Identify the blood parasite species.
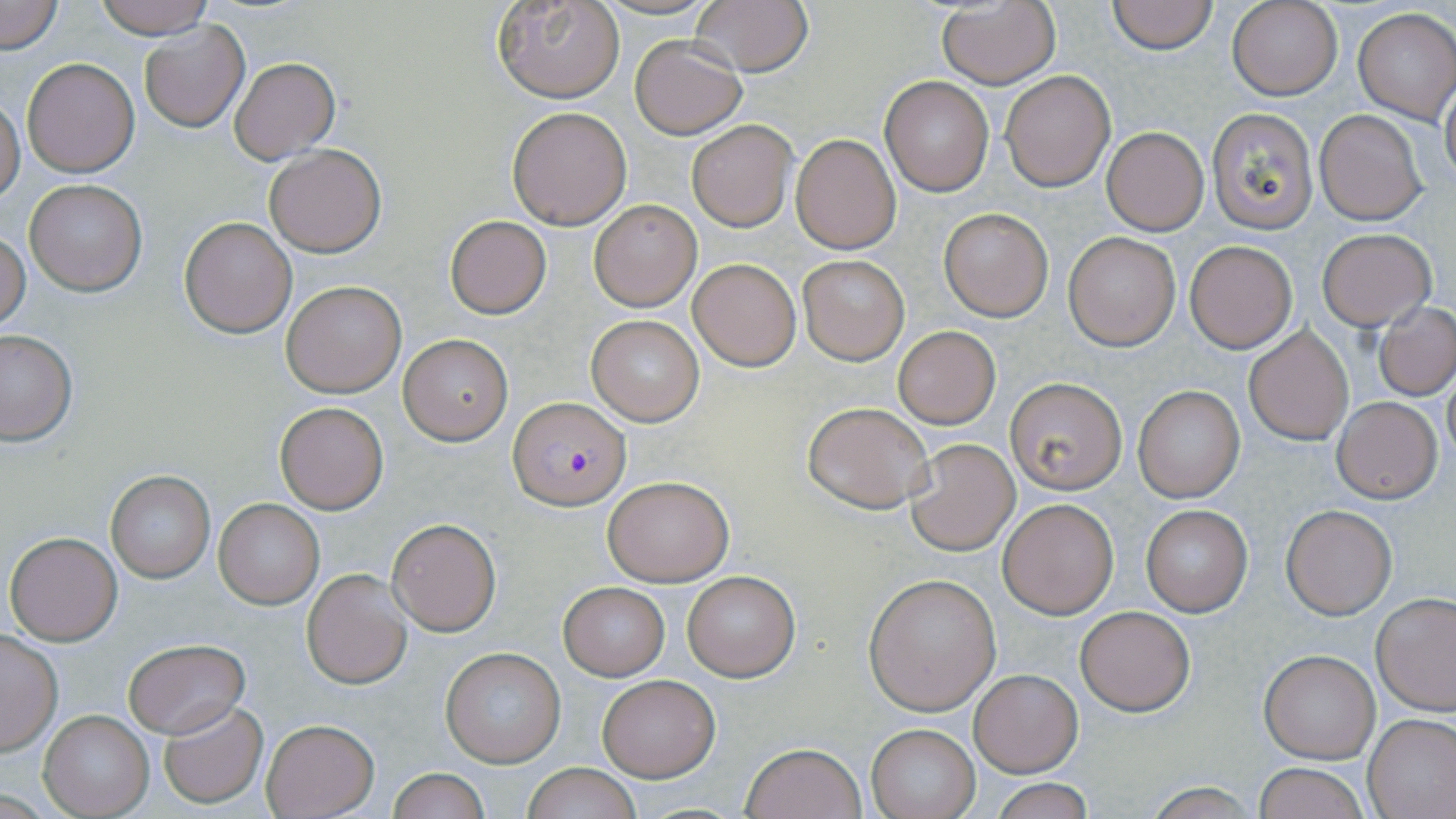
Plasmodium falciparum.

magnification = 1000x
uninfected red blood cell locations = approximate bounding boxes as named x1/y1/x2/y2 corners in pixels: (x1=1, y1=0, x2=65, y2=55), (x1=94, y1=0, x2=216, y2=40), (x1=1108, y1=0, x2=1216, y2=54), (x1=496, y1=1, x2=623, y2=103), (x1=690, y1=1, x2=814, y2=77), (x1=1227, y1=1, x2=1342, y2=100), (x1=937, y1=3, x2=1061, y2=87), (x1=1353, y1=8, x2=1455, y2=122), (x1=140, y1=21, x2=249, y2=132), (x1=630, y1=37, x2=747, y2=138), (x1=22, y1=58, x2=140, y2=176), (x1=230, y1=58, x2=339, y2=162), (x1=1001, y1=69, x2=1116, y2=192), (x1=880, y1=76, x2=995, y2=196), (x1=1440, y1=78, x2=1456, y2=191), (x1=0, y1=94, x2=25, y2=207), (x1=506, y1=106, x2=633, y2=229), (x1=1206, y1=108, x2=1318, y2=233), (x1=1314, y1=109, x2=1428, y2=225), (x1=687, y1=120, x2=795, y2=231), (x1=1102, y1=126, x2=1208, y2=235), (x1=790, y1=133, x2=900, y2=255), (x1=263, y1=143, x2=387, y2=257), (x1=22, y1=178, x2=146, y2=296), (x1=587, y1=198, x2=703, y2=311), (x1=938, y1=208, x2=1053, y2=321), (x1=445, y1=215, x2=551, y2=318), (x1=179, y1=217, x2=296, y2=338), (x1=1, y1=229, x2=30, y2=332), (x1=1316, y1=229, x2=1435, y2=330), (x1=1063, y1=230, x2=1182, y2=351), (x1=1185, y1=240, x2=1297, y2=353), (x1=797, y1=253, x2=910, y2=365), (x1=688, y1=257, x2=800, y2=370), (x1=281, y1=280, x2=405, y2=396), (x1=1373, y1=301, x2=1456, y2=401), (x1=587, y1=315, x2=705, y2=426), (x1=893, y1=325, x2=1001, y2=430), (x1=1243, y1=325, x2=1353, y2=445), (x1=0, y1=330, x2=77, y2=446), (x1=398, y1=333, x2=513, y2=444), (x1=1441, y1=366, x2=1456, y2=467), (x1=1004, y1=377, x2=1127, y2=494), (x1=1133, y1=386, x2=1245, y2=502), (x1=1333, y1=397, x2=1442, y2=502), (x1=274, y1=401, x2=390, y2=515), (x1=802, y1=401, x2=933, y2=513), (x1=906, y1=437, x2=1020, y2=555), (x1=104, y1=469, x2=215, y2=583), (x1=603, y1=474, x2=732, y2=586), (x1=998, y1=498, x2=1118, y2=619), (x1=213, y1=499, x2=323, y2=608), (x1=1141, y1=505, x2=1253, y2=616), (x1=1281, y1=505, x2=1397, y2=619), (x1=388, y1=518, x2=500, y2=636), (x1=6, y1=531, x2=123, y2=645), (x1=302, y1=569, x2=412, y2=688), (x1=683, y1=572, x2=800, y2=681), (x1=864, y1=575, x2=1001, y2=714), (x1=559, y1=583, x2=669, y2=679), (x1=1372, y1=592, x2=1456, y2=715), (x1=1075, y1=605, x2=1195, y2=715), (x1=0, y1=633, x2=62, y2=755), (x1=122, y1=637, x2=251, y2=740), (x1=441, y1=646, x2=567, y2=768), (x1=1258, y1=649, x2=1380, y2=764), (x1=970, y1=669, x2=1081, y2=777), (x1=596, y1=674, x2=720, y2=783), (x1=158, y1=700, x2=269, y2=807), (x1=41, y1=710, x2=153, y2=817), (x1=1365, y1=713, x2=1456, y2=818), (x1=261, y1=719, x2=379, y2=818), (x1=866, y1=724, x2=979, y2=819), (x1=741, y1=743, x2=867, y2=819), (x1=1253, y1=763, x2=1369, y2=819), (x1=522, y1=764, x2=641, y2=819), (x1=388, y1=767, x2=489, y2=819), (x1=990, y1=780, x2=1097, y2=819)
image size = 1456×819 pixels
field of view = one of a larger specimen
preparation = thin blood smear
stain = May-Grünwald-Giemsa
Plasmodium falciparum-infected red blood cell locations = approximate bounding boxes as named x1/y1/x2/y2 corners in pixels: (x1=509, y1=398, x2=630, y2=510)
modality = optical microscopy